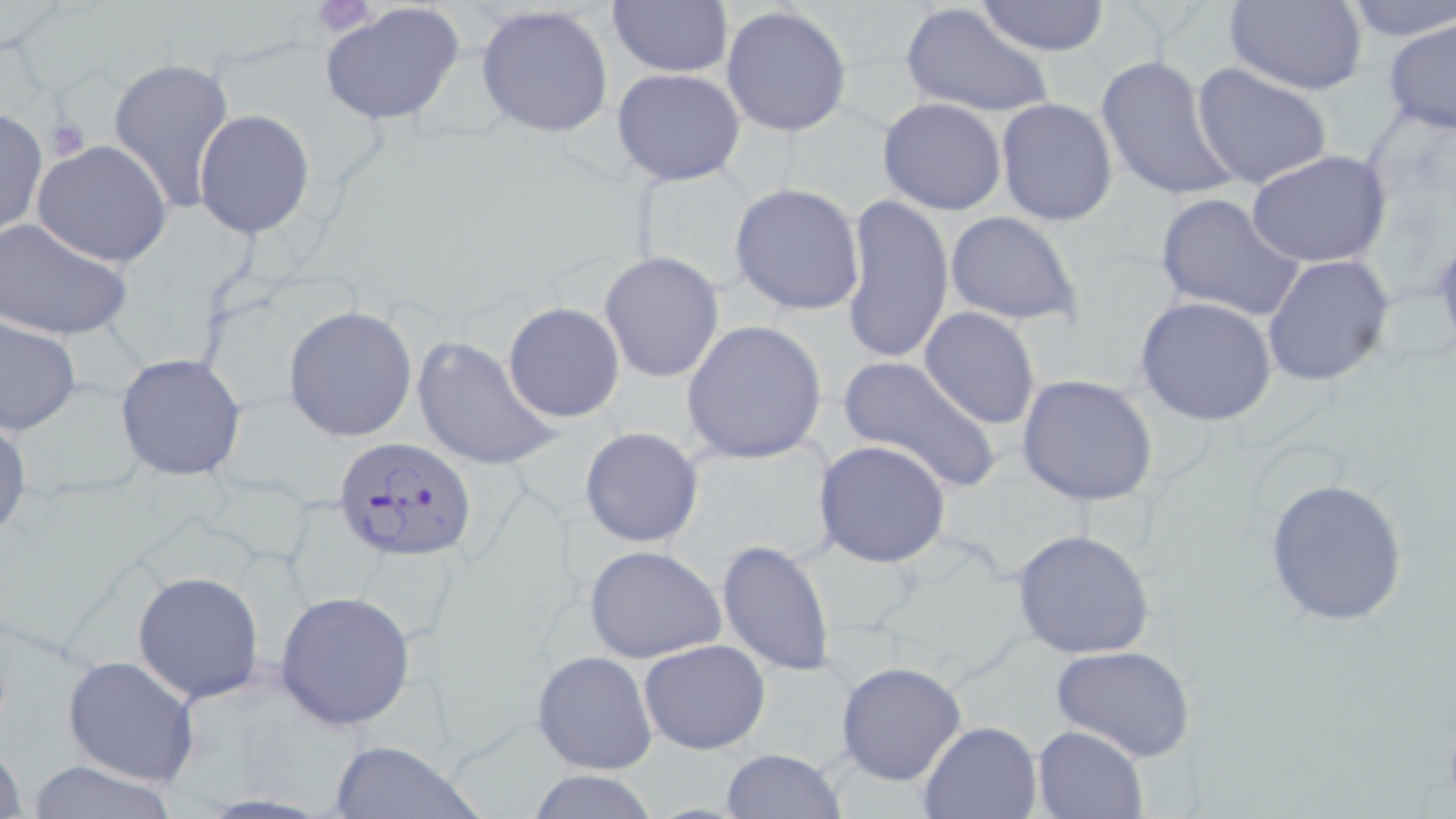

slide_level_diagnosis: Plasmodium falciparum
field_of_view: single
uninfected_red_blood_cell_locations: 'approximate bounding boxes as named x1/y1/x2/y2 corners in pixels: (x1=976, y1=0, x2=1110, y2=56), (x1=1224, y1=0, x2=1368, y2=95), (x1=1341, y1=0, x2=1455, y2=39), (x1=607, y1=1, x2=734, y2=78), (x1=318, y1=2, x2=466, y2=128), (x1=475, y1=4, x2=617, y2=140), (x1=721, y1=4, x2=854, y2=139), (x1=900, y1=4, x2=1054, y2=120), (x1=1383, y1=15, x2=1456, y2=137), (x1=1093, y1=53, x2=1239, y2=204), (x1=106, y1=54, x2=234, y2=213), (x1=1192, y1=63, x2=1332, y2=190), (x1=612, y1=68, x2=748, y2=186), (x1=877, y1=97, x2=1007, y2=216), (x1=995, y1=97, x2=1118, y2=227), (x1=0, y1=107, x2=47, y2=238), (x1=193, y1=109, x2=315, y2=240), (x1=30, y1=139, x2=174, y2=268), (x1=1245, y1=150, x2=1392, y2=270), (x1=729, y1=182, x2=865, y2=317), (x1=1153, y1=193, x2=1306, y2=321), (x1=840, y1=195, x2=953, y2=366), (x1=944, y1=212, x2=1083, y2=326), (x1=0, y1=217, x2=134, y2=343), (x1=599, y1=251, x2=725, y2=382), (x1=1261, y1=253, x2=1395, y2=387), (x1=1133, y1=296, x2=1279, y2=427), (x1=503, y1=302, x2=626, y2=423), (x1=283, y1=305, x2=418, y2=442), (x1=918, y1=306, x2=1041, y2=430), (x1=1, y1=315, x2=81, y2=435), (x1=680, y1=320, x2=828, y2=466), (x1=410, y1=334, x2=558, y2=473), (x1=115, y1=353, x2=248, y2=482), (x1=835, y1=355, x2=1002, y2=493), (x1=1016, y1=374, x2=1160, y2=507), (x1=0, y1=411, x2=31, y2=546), (x1=580, y1=426, x2=703, y2=547), (x1=812, y1=440, x2=952, y2=569), (x1=1261, y1=477, x2=1410, y2=626), (x1=1009, y1=529, x2=1156, y2=661), (x1=715, y1=538, x2=836, y2=675), (x1=584, y1=545, x2=729, y2=664), (x1=133, y1=570, x2=265, y2=704), (x1=274, y1=590, x2=417, y2=730), (x1=637, y1=639, x2=770, y2=755), (x1=1048, y1=644, x2=1198, y2=763), (x1=531, y1=649, x2=657, y2=775), (x1=62, y1=655, x2=199, y2=787), (x1=833, y1=661, x2=968, y2=785), (x1=916, y1=720, x2=1042, y2=819), (x1=1031, y1=724, x2=1149, y2=818), (x1=0, y1=735, x2=27, y2=819), (x1=327, y1=740, x2=484, y2=819), (x1=721, y1=748, x2=846, y2=818), (x1=20, y1=760, x2=184, y2=818), (x1=528, y1=770, x2=659, y2=819)'
platelet_locations: 'approximate bounding boxes as named x1/y1/x2/y2 corners in pixels: (x1=45, y1=117, x2=91, y2=160)'
stain: May-Grünwald-Giemsa
plasmodium_falciparum_infected_red_blood_cell_locations: 'approximate bounding boxes as named x1/y1/x2/y2 corners in pixels: (x1=334, y1=435, x2=479, y2=563)'
magnification: 1000x
modality: optical microscopy
image_size: 1456×819 pixels
preparation: thin blood film